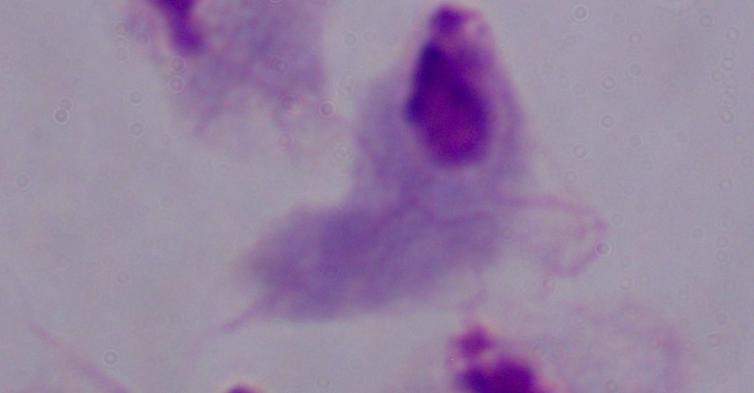 Photomicrograph. Captured at 1000x magnification. A trichomonad is seen.